Comment on the morphology of the red blood cells.
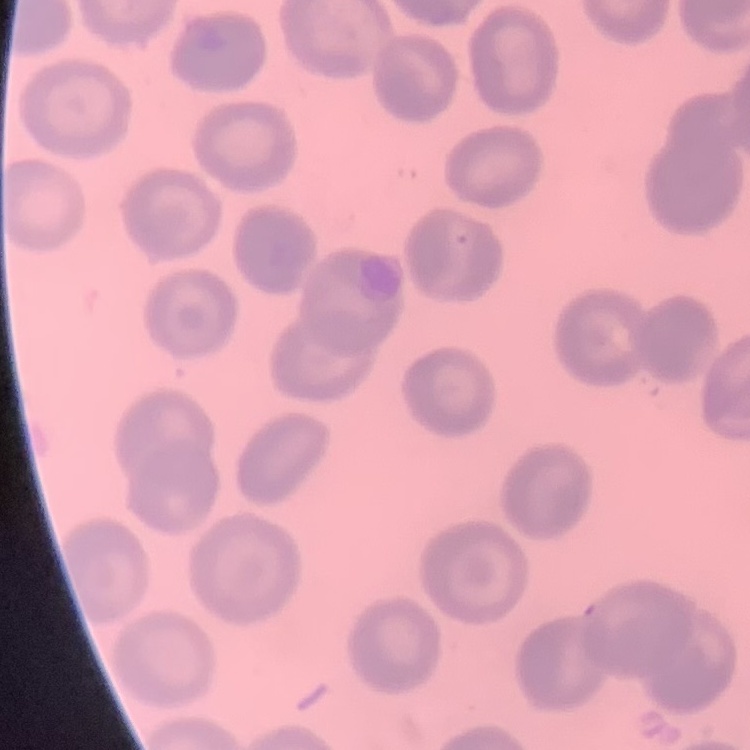

They show no rouleaux formation.

Summary:
  - Stain: Field's or Giemsa
  - Image type: square crop of a larger photomicrograph
  - Preparation: thin peripheral smear